Give the position of every Plasmodium parasite.
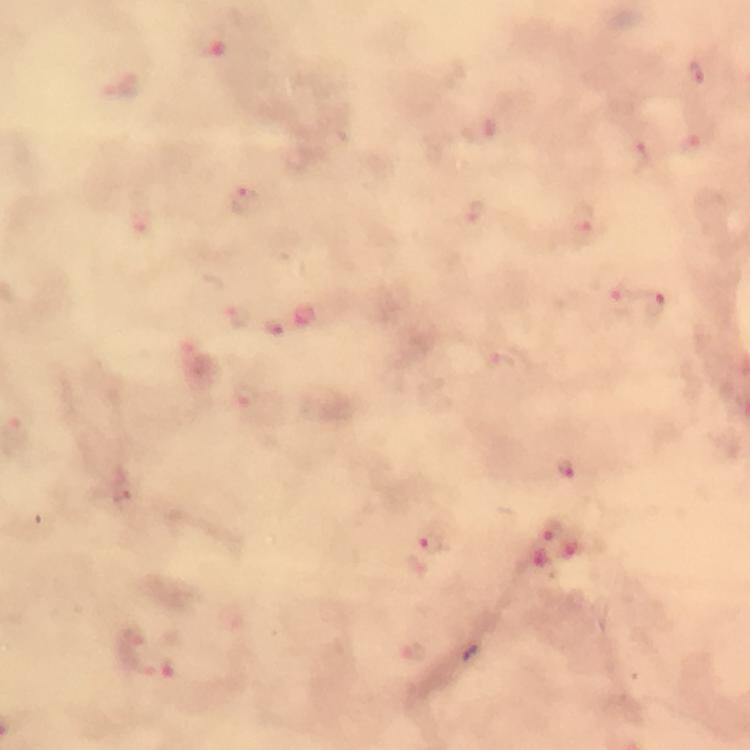
Approximate centers as [x, y] in pixels.
Plasmodium parasites: [210, 46], [694, 72], [480, 132], [693, 147], [638, 151], [245, 202], [474, 211], [583, 223], [614, 300], [649, 305], [234, 316], [277, 328], [497, 362], [245, 394], [567, 467], [128, 492], [551, 532], [430, 544], [132, 640].

Image is 750×750 pixels. A crop from one field of view. Smartphone photograph taken through a microscope. Giemsa-stained preparation. Immersion oil was used. Thick smear. From a diagnostic examination for malaria. 100x magnification.